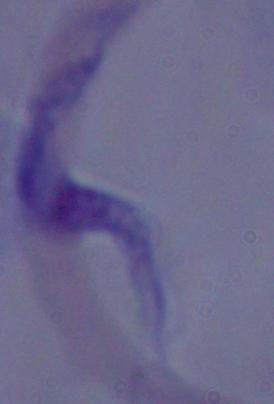

{
  "modality": "micrograph",
  "identification": "trypanosome",
  "magnification": "1000x"
}